Identify the parasite.
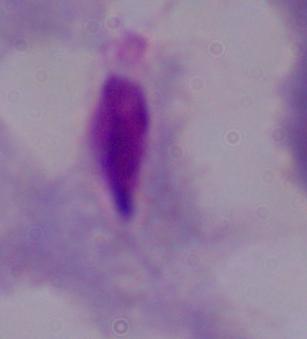
This is a trichomonad.

Summary:
  - Magnification: 1000x
  - Modality: photomicrograph